Locate every uninfected red blood cell.
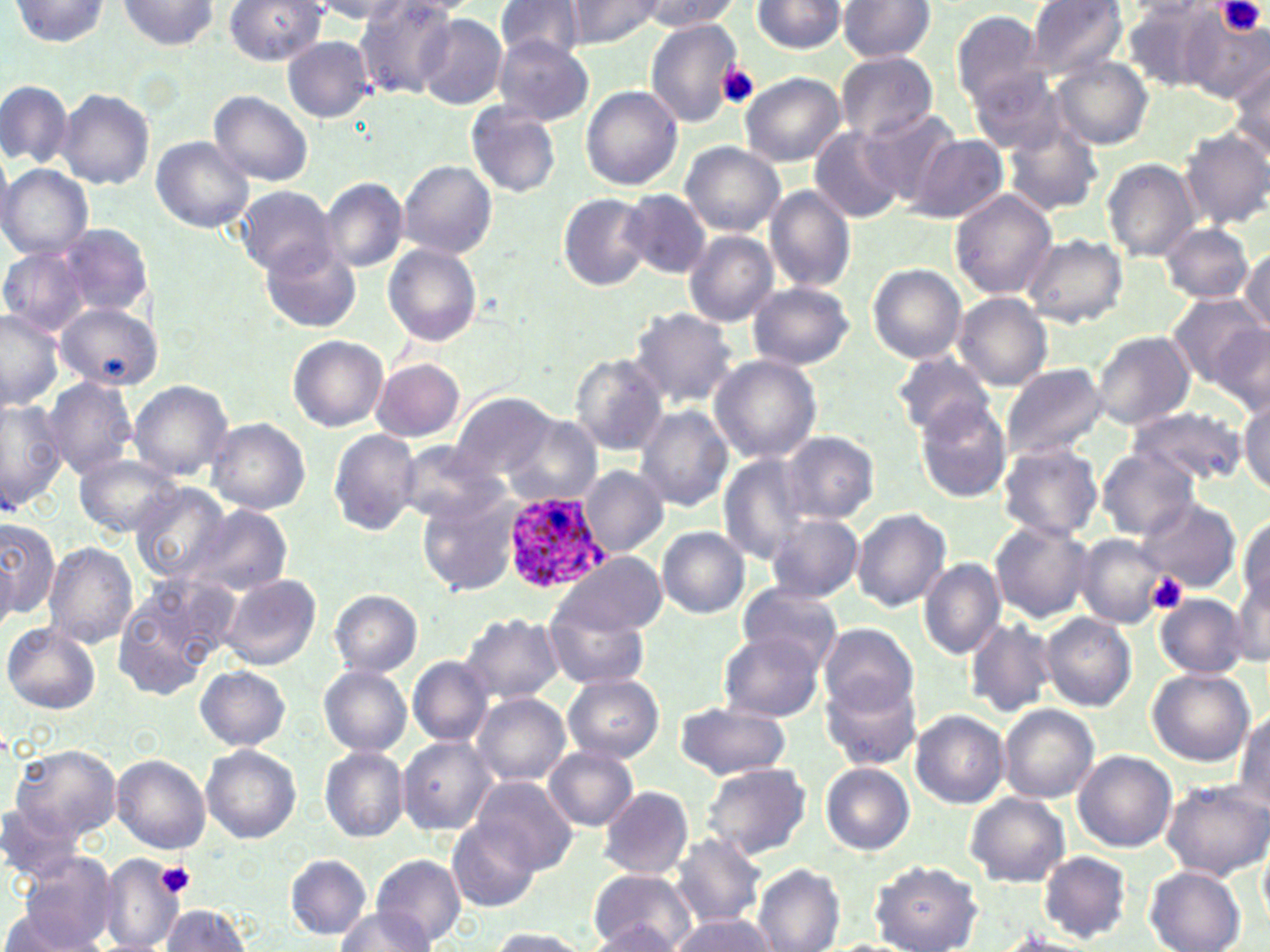
Approximate bounding boxes as [x1, y1, x2, y2] in pixels.
Uninfected red blood cells: [118, 0, 219, 49], [225, 0, 325, 64], [355, 0, 459, 99], [496, 0, 591, 63], [563, 0, 668, 48], [639, 0, 738, 30], [1026, 0, 1130, 79], [10, 1, 112, 48], [308, 1, 413, 22], [750, 1, 850, 55], [836, 1, 937, 62], [1119, 2, 1226, 92], [950, 8, 1046, 109], [1178, 8, 1270, 103], [415, 14, 507, 110], [645, 18, 745, 128], [282, 37, 375, 121], [494, 37, 596, 125], [835, 52, 939, 140], [1227, 52, 1270, 160], [1053, 57, 1154, 151], [969, 66, 1069, 155], [739, 71, 844, 167], [0, 80, 71, 167], [581, 85, 683, 190], [55, 89, 153, 190], [210, 91, 314, 185], [467, 102, 563, 198], [860, 108, 962, 204], [1004, 124, 1102, 216], [809, 126, 908, 224], [1178, 126, 1270, 231], [909, 134, 1008, 224], [150, 137, 253, 232], [680, 142, 786, 236], [1103, 158, 1200, 263], [398, 160, 498, 261], [0, 164, 94, 261], [321, 179, 408, 273], [233, 185, 340, 278], [765, 185, 856, 294], [621, 189, 711, 279], [949, 189, 1057, 299], [558, 193, 655, 292], [58, 222, 154, 323], [1158, 222, 1257, 303], [682, 230, 779, 327], [1019, 233, 1127, 328], [264, 244, 360, 333], [384, 244, 482, 346], [0, 245, 91, 337], [1239, 246, 1270, 336], [866, 263, 967, 364], [748, 283, 856, 371], [1165, 292, 1268, 392], [954, 293, 1052, 388], [57, 302, 160, 391], [628, 308, 739, 408], [0, 309, 65, 410], [1209, 326, 1268, 413], [1093, 331, 1196, 430], [289, 335, 388, 431], [891, 350, 995, 440], [568, 354, 670, 456], [710, 355, 823, 463], [371, 358, 465, 443], [1000, 362, 1109, 462], [43, 378, 137, 477], [127, 380, 232, 478], [452, 391, 555, 483], [1239, 394, 1269, 500], [0, 398, 68, 509], [915, 401, 1011, 503], [635, 406, 734, 511], [1128, 406, 1245, 488], [500, 416, 603, 506], [207, 417, 311, 515], [328, 429, 422, 535], [780, 431, 878, 524], [393, 441, 506, 526], [997, 442, 1104, 542], [1096, 448, 1200, 541], [75, 452, 183, 538], [717, 455, 816, 564], [581, 467, 669, 557], [131, 482, 229, 580], [421, 495, 520, 595], [1139, 497, 1242, 593], [183, 503, 294, 598], [851, 508, 951, 612], [766, 512, 862, 602], [1237, 512, 1269, 616], [0, 516, 59, 622], [990, 520, 1093, 622], [658, 526, 751, 618], [1076, 534, 1164, 628], [42, 540, 138, 648], [552, 553, 667, 636], [918, 558, 1006, 658], [1232, 568, 1268, 666], [220, 573, 321, 671], [738, 581, 845, 668], [113, 583, 227, 699], [329, 590, 422, 676], [1154, 594, 1248, 677], [545, 602, 650, 690], [460, 612, 563, 706], [1043, 613, 1137, 711], [964, 615, 1057, 718], [3, 623, 99, 714], [818, 624, 918, 718], [718, 632, 824, 721], [407, 656, 495, 747], [319, 663, 411, 756], [197, 666, 290, 750], [1146, 667, 1257, 768], [564, 675, 664, 762], [822, 679, 920, 771], [472, 692, 571, 787], [674, 702, 791, 780], [998, 704, 1098, 803], [910, 709, 1009, 808], [1234, 709, 1268, 810], [398, 736, 496, 835], [9, 742, 123, 848], [202, 745, 300, 842], [319, 746, 408, 842], [543, 746, 639, 831], [1073, 750, 1176, 852], [112, 755, 211, 852], [701, 762, 813, 860], [821, 763, 915, 854], [473, 776, 577, 872], [1160, 779, 1270, 880], [597, 785, 694, 879], [966, 793, 1071, 887], [2, 801, 82, 881], [448, 818, 541, 912], [668, 830, 768, 928], [1258, 838, 1270, 927], [1039, 851, 1132, 943], [98, 852, 185, 952], [13, 853, 120, 950], [285, 854, 372, 939], [372, 854, 466, 949], [870, 861, 983, 952], [753, 864, 845, 952], [1145, 867, 1246, 952], [587, 869, 695, 952], [0, 905, 101, 952], [161, 905, 250, 952], [332, 907, 438, 951], [666, 915, 777, 952], [591, 922, 686, 950], [486, 929, 591, 951], [825, 939, 920, 952].

Plasmodium ovale-infected red blood cell locations: [501, 493, 612, 594]. Platelet locations: [1220, 0, 1267, 37], [717, 64, 760, 108], [1147, 573, 1187, 614], [157, 862, 195, 897]. Slide-level diagnosis: Plasmodium ovale. Single field of view. Thin blood smear. Image is 1270×952 pixels. May-Grünwald-Giemsa-stained preparation. Light microscopy. Captured at 1000x magnification.